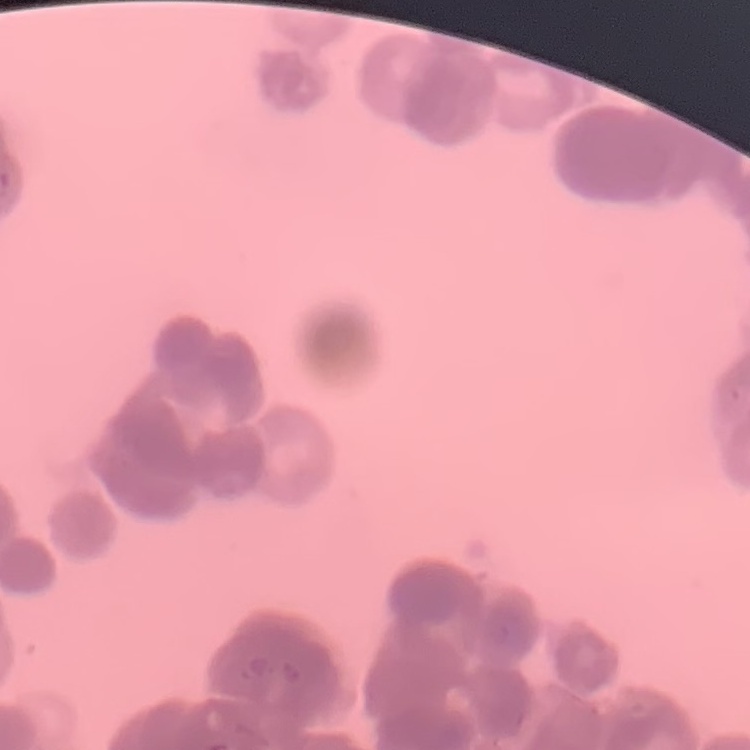

Summary:
  - Erythrocyte morphology: rouleaux formation
  - Stain: Field's or Giemsa
  - Image type: one tile cut from a larger photomicrograph
  - Preparation: thin peripheral smear